Draw a bounding box around every leukocyte (white blood cell).
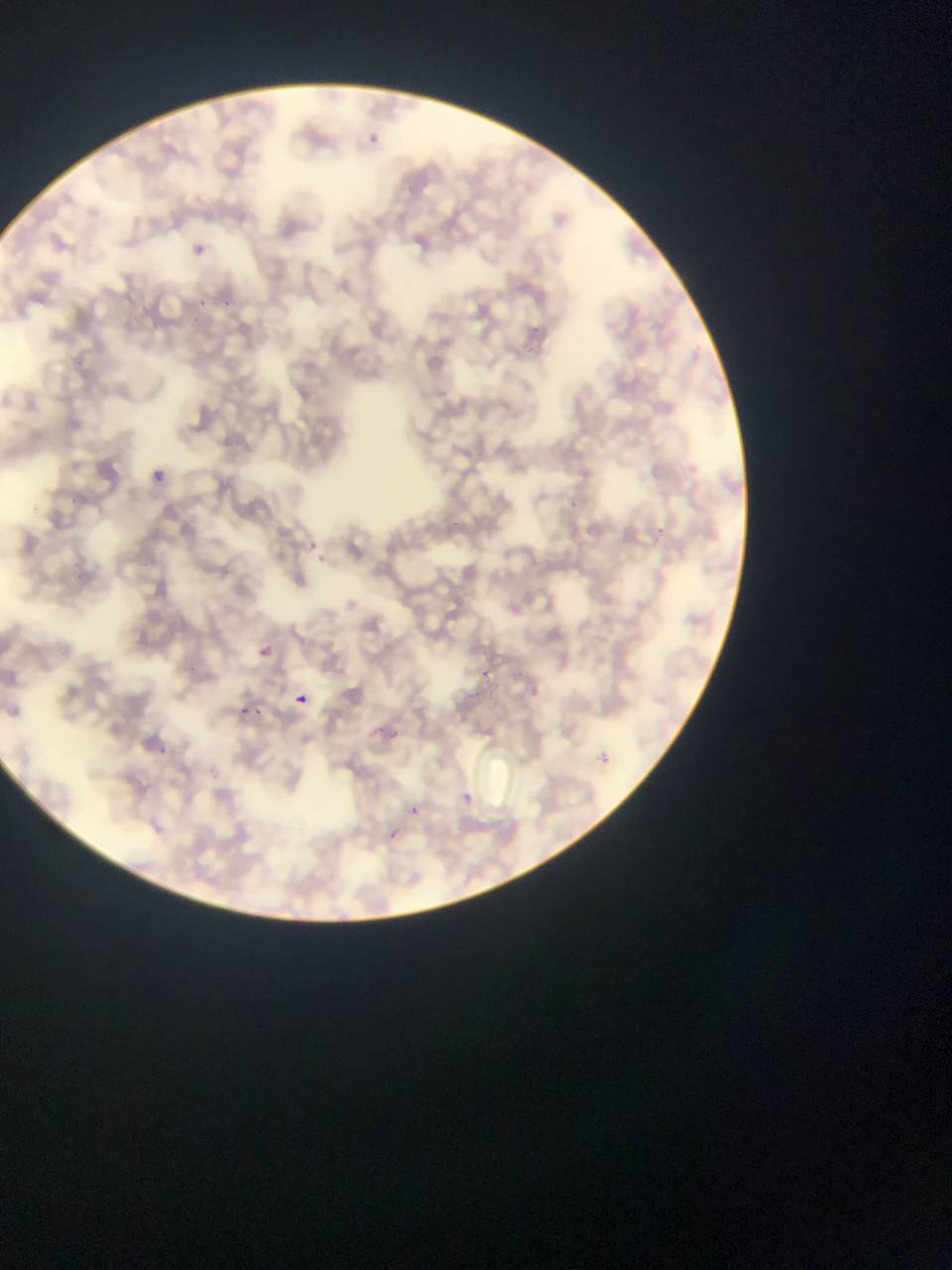

No leukocytes observed.

Approximate bounding boxes as {left, top, right, bottom} in pixels.
Summary:
  - Plasmodium parasite locations: {362, 130, 385, 151}, {182, 241, 212, 254}, {195, 292, 229, 317}, {151, 463, 177, 485}, {308, 538, 317, 544}, {313, 551, 331, 568}, {256, 638, 274, 659}, {296, 694, 308, 706}, {237, 704, 264, 721}, {383, 724, 409, 749}, {154, 739, 183, 762}, {590, 748, 626, 773}, {456, 791, 487, 804}, {406, 800, 432, 817}, {374, 822, 404, 840}
  - Preparation: thin blood film
  - Image size: 952×1270 pixels
  - Field of view: single
  - Country: Ghana
  - Capture: mobile-phone photograph through a microscope